Describe the morphology of the erythrocytes.
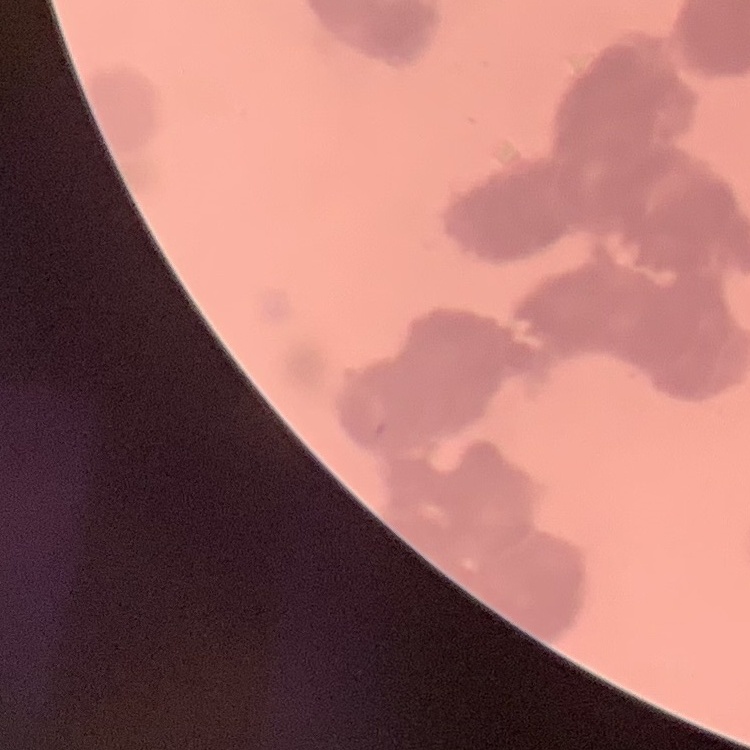
Rouleaux formation.

One tile cut from a larger photomicrograph. Stained with either Field's or Giemsa. Thin peripheral smear.